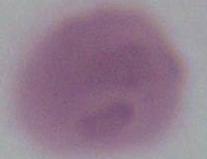

magnification: 1000x
identification: red blood cell
modality: photomicrograph